Classify this cell by malaria status.
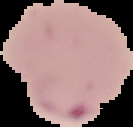
Parasitized.

From a thin blood smear. Image is 133×127 pixels. The area outside the segmented cell region is set to black.